State which parasite is depicted.
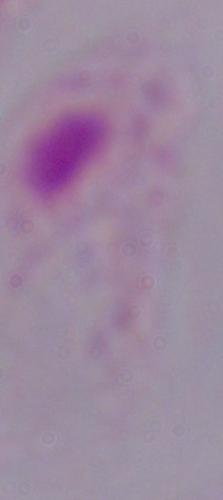

This is a trichomonad.

Photomicrograph. 1000x magnification.